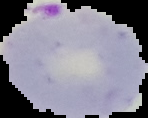
Result: malaria parasites identified. From a thin blood film. The area outside the segmented cell region is set to black. Image is 148×118 pixels.